Give the position of every Plasmodium parasite.
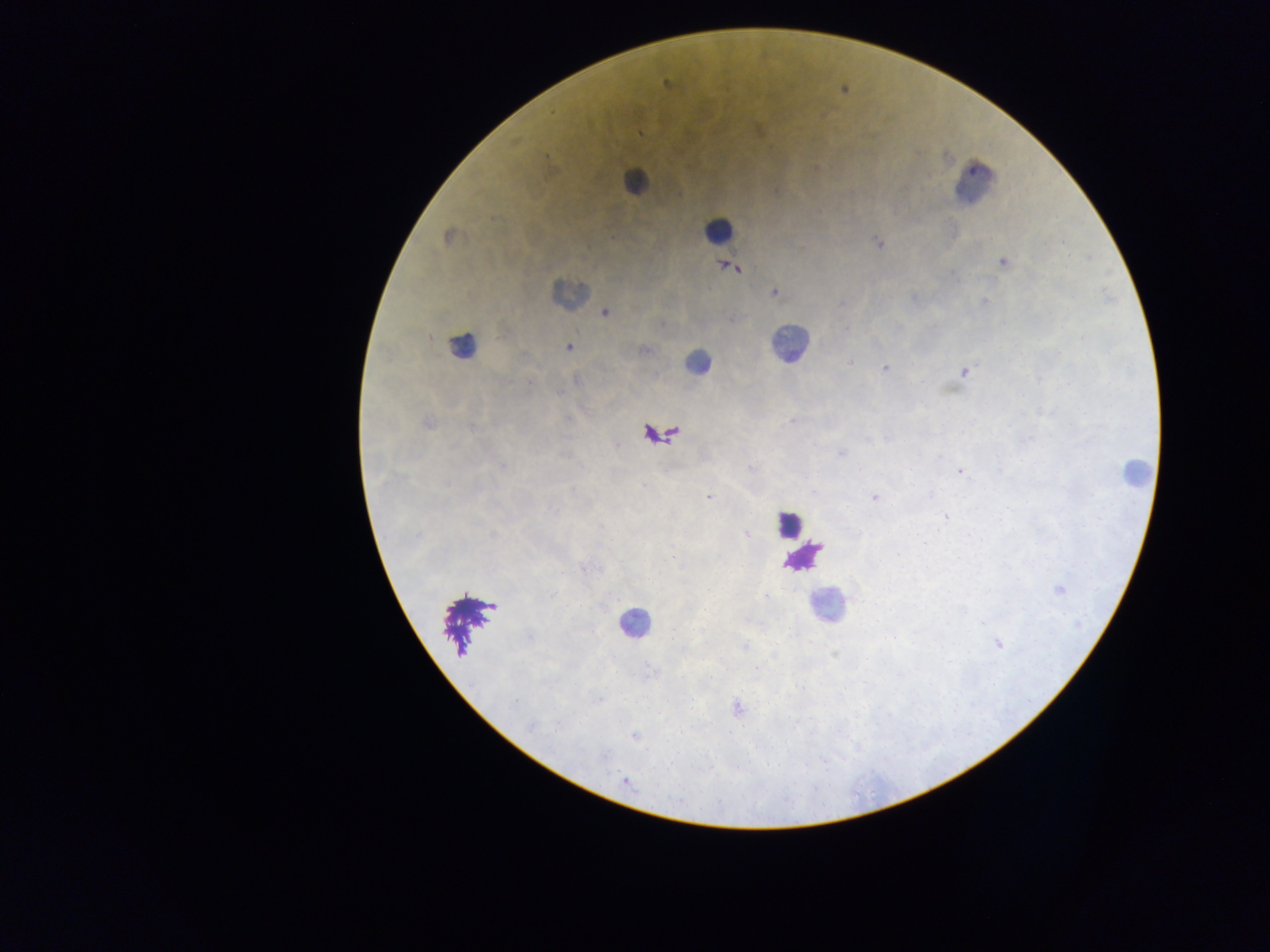
Approximate centers as (x, y) in pixels.
Plasmodium parasites: (667, 84), (758, 131), (639, 134), (447, 236), (877, 242), (1063, 243), (1003, 262), (733, 268), (953, 273), (774, 293), (914, 298), (984, 302), (842, 303), (605, 313), (734, 319), (845, 331), (569, 347), (644, 350), (851, 362), (885, 369), (964, 373), (576, 380), (530, 382), (569, 420), (792, 421), (428, 423), (471, 428), (869, 440), (841, 454), (751, 468), (859, 470), (960, 471), (644, 485), (708, 497), (875, 497), (945, 518), (601, 526), (746, 534), (492, 536), (670, 556), (583, 568), (1058, 589), (766, 597), (705, 610), (983, 623), (530, 637), (998, 645), (744, 646), (756, 668), (651, 669), (599, 699), (515, 702), (737, 707), (559, 726), (532, 728), (635, 737), (625, 781).

country = Ghana
capture = mobile-phone photograph through a microscope
preparation = thick blood film
image size = 1270×952 pixels
field of view = single
leukocyte locations = approximate centers as (x, y) in pixels: (634, 182), (975, 186), (718, 230), (568, 294), (789, 344), (463, 345), (698, 363), (1135, 471), (788, 523), (826, 606), (634, 623)